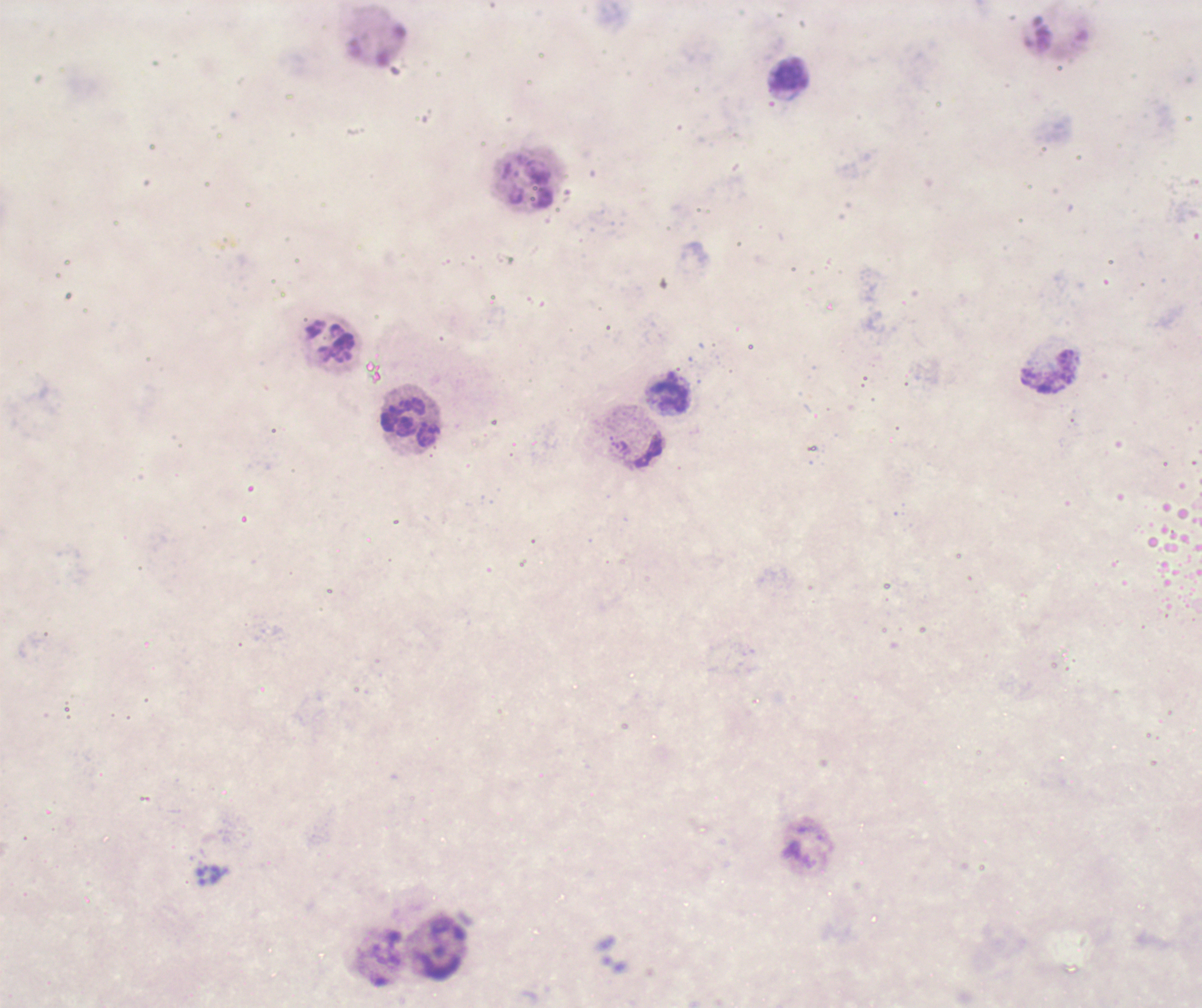
Approximate centers as {x, y} in pixels. Leukocyte locations: {789, 76}, {529, 181}, {330, 343}, {1050, 371}, {671, 397}, {409, 421}. One field from this slide. Coloration quality: bad. Result: negative for Plasmodium parasites. Thick smear of blood. Romanowsky-stained preparation. Image is 1202×1008 pixels. Background quality: unsatisfactory. 100x magnification. Previously used in a real diagnosis.